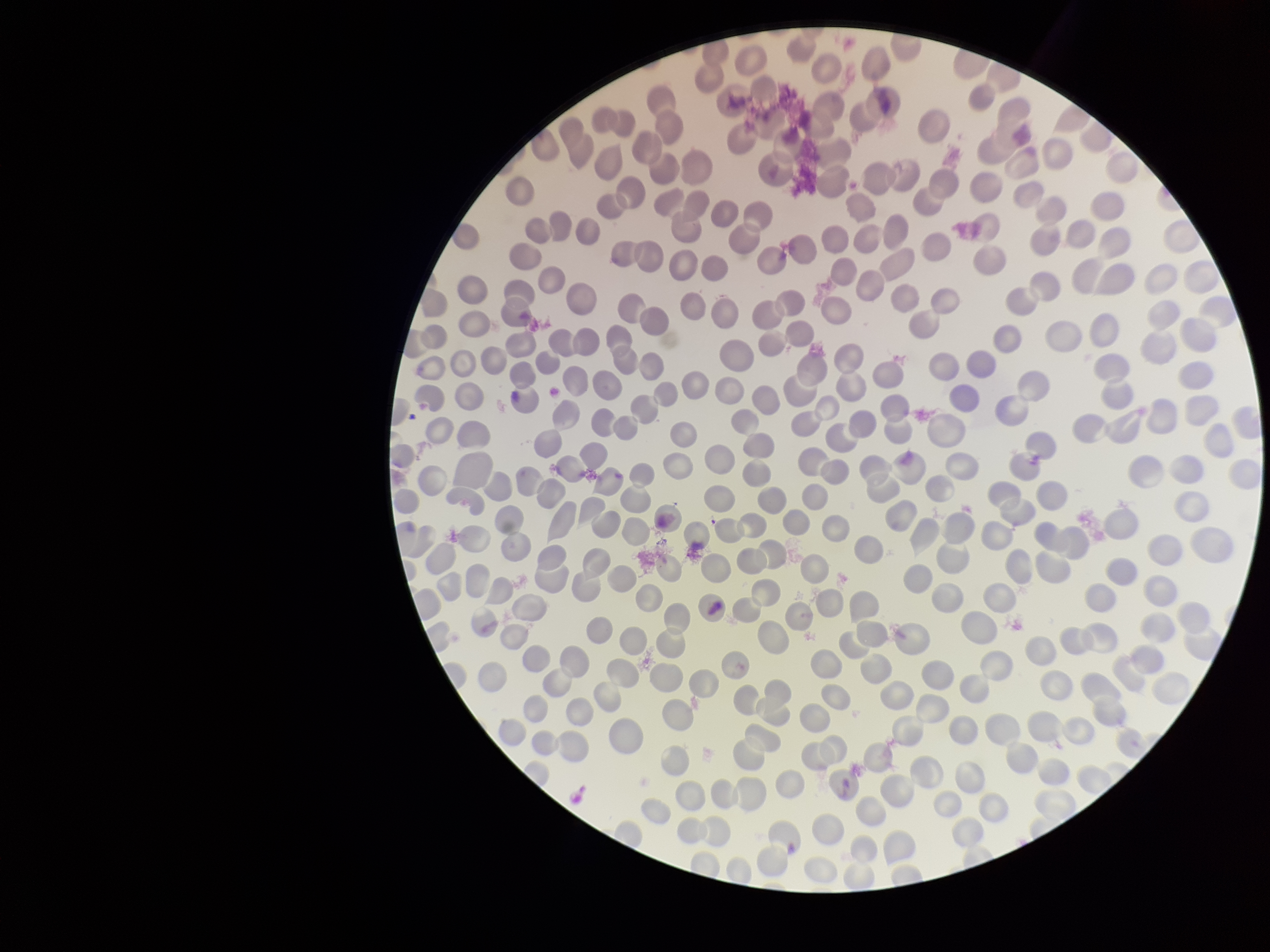

field of view = single
parasitized red blood cells = none seen
capture = smartphone photograph through the microscope eyepiece
red blood cell count = 265
preparation = thin
patient malaria status = negative
image size = 1270×952 pixels
parasitized red blood cell count = 0
stain = Giemsa